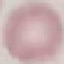
Summary:
  - Malaria status: uninfected
  - Capture: smartphone camera at the microscope eyepiece
  - Image type: automatically extracted cell patch, resized to 64 × 64 pixels
  - Stain: Giemsa
  - Preparation: thin blood smear